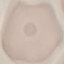
Malaria status: uninfected. Thin blood smear. Cell patch, automatically extracted from a larger field of view and resized to 64 × 64 pixels. Giemsa stain. Photographed with a smartphone camera at the microscope eyepiece.